Report the malaria status of this cell.
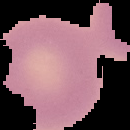
It is uninfected.

Summary:
  - Preparation: thin blood smear
  - Image type: segmented cell region on a black background
  - Image size: 130×130 pixels